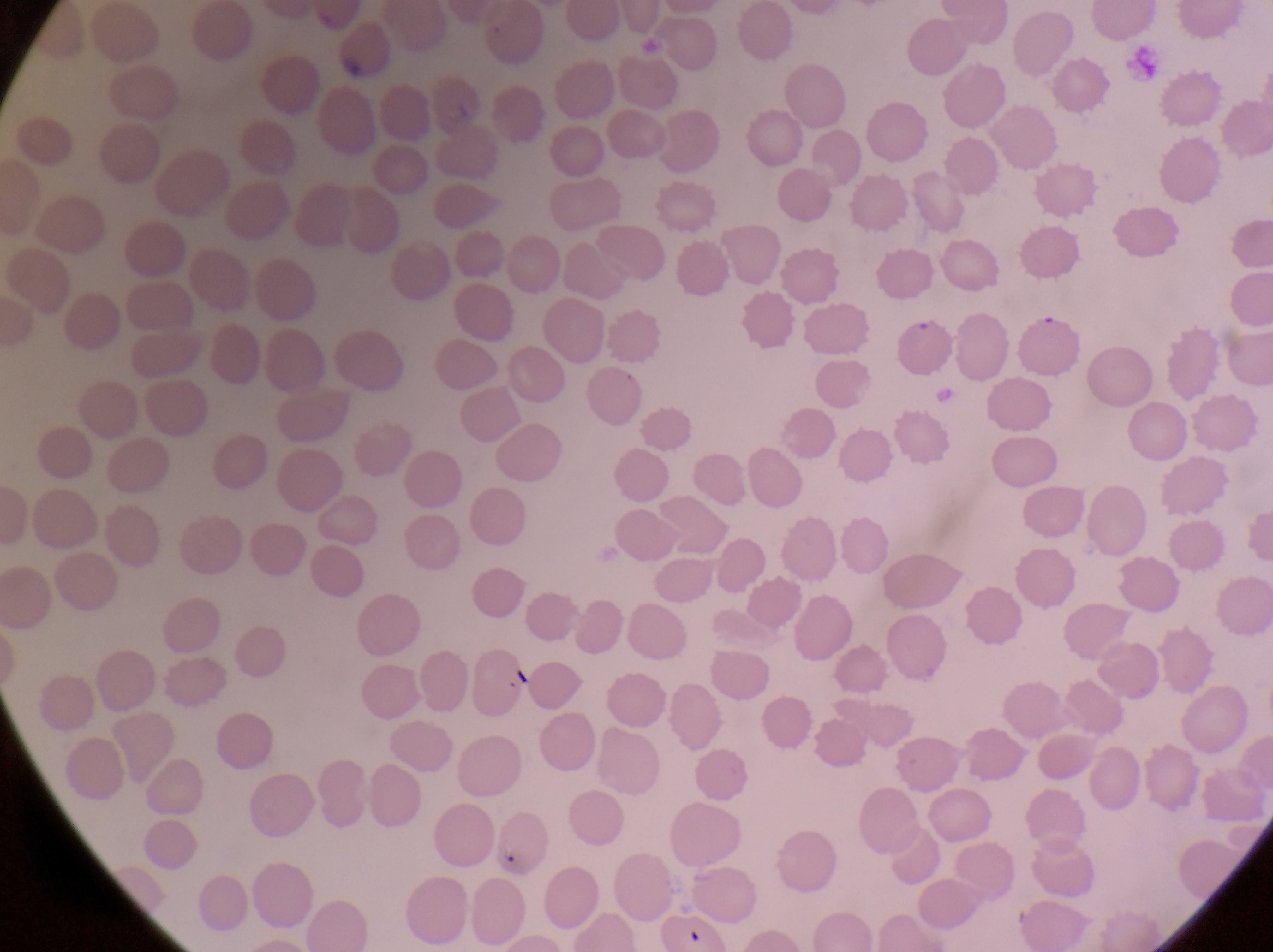

Approximate bounding boxes as {left, top, right, bottom} in pixels.
Summary:
  - Parasitised red blood cell locations: {1021, 312, 1090, 370}
  - Artifact (platelet-like body, stain precipitate, or debris) locations: {505, 659, 544, 698}
  - Magnification: 1000x
  - Field of view: single
  - Country: Uganda
  - Image size: 1273×952 pixels
  - Preparation: thin blood smear
  - Capture: smartphone photograph through the eyepiece of an Olympus CX-23 microscope